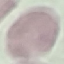
Summary:
  - Malaria status: uninfected
  - Image type: cell patch, automatically extracted from a larger field of view and resized to 64 × 64 pixels
  - Capture: smartphone through the microscope eyepiece
  - Stain: Giemsa
  - Preparation: thin smear